Assess for malaria.
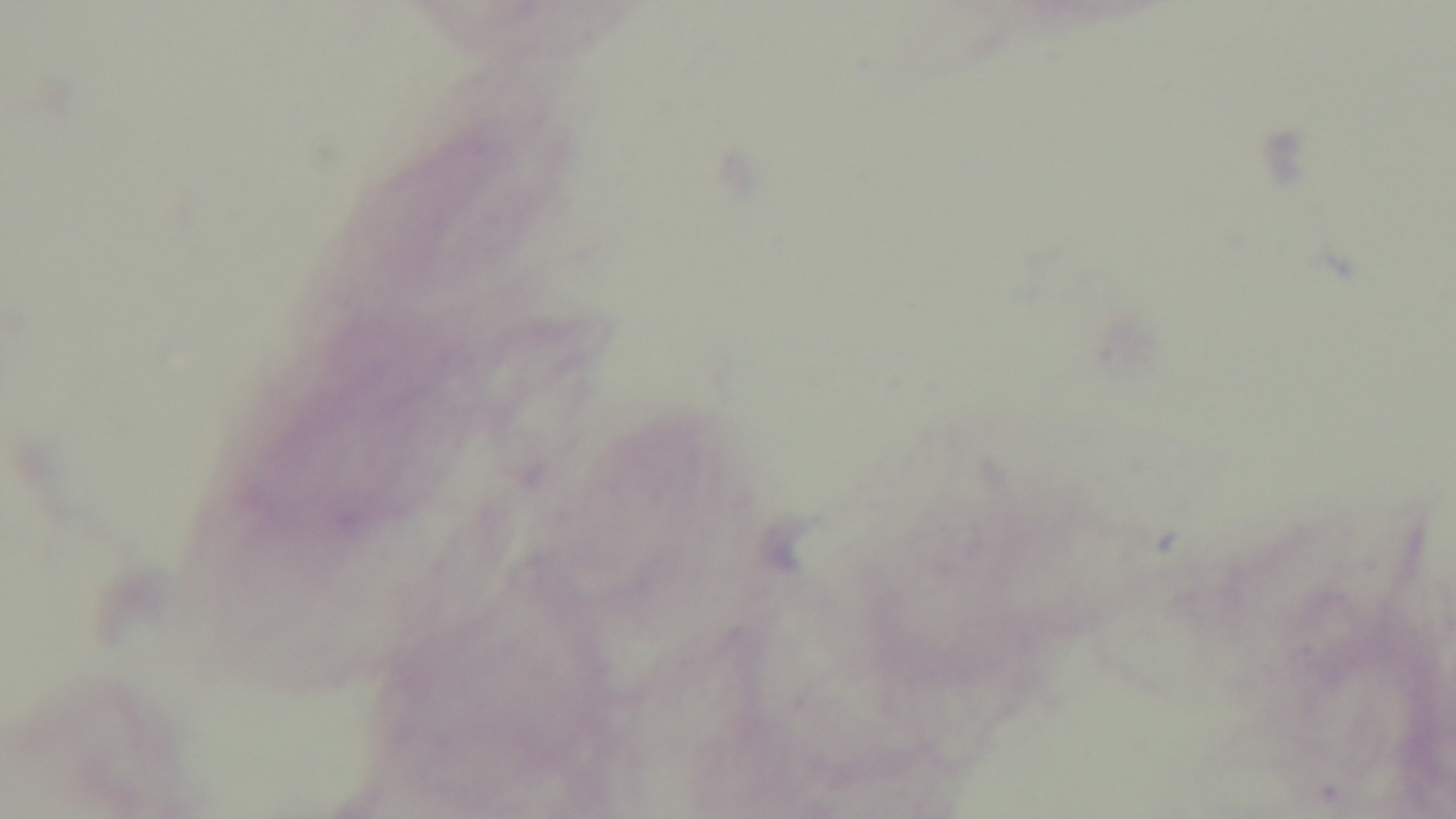

Negative.

stain = Giemsa
field of view = single
capture = mounted 4K digital camera
objective = 100x oil immersion
preparation = thick smear
modality = light microscopy